Assess the morphology of the red blood cells.
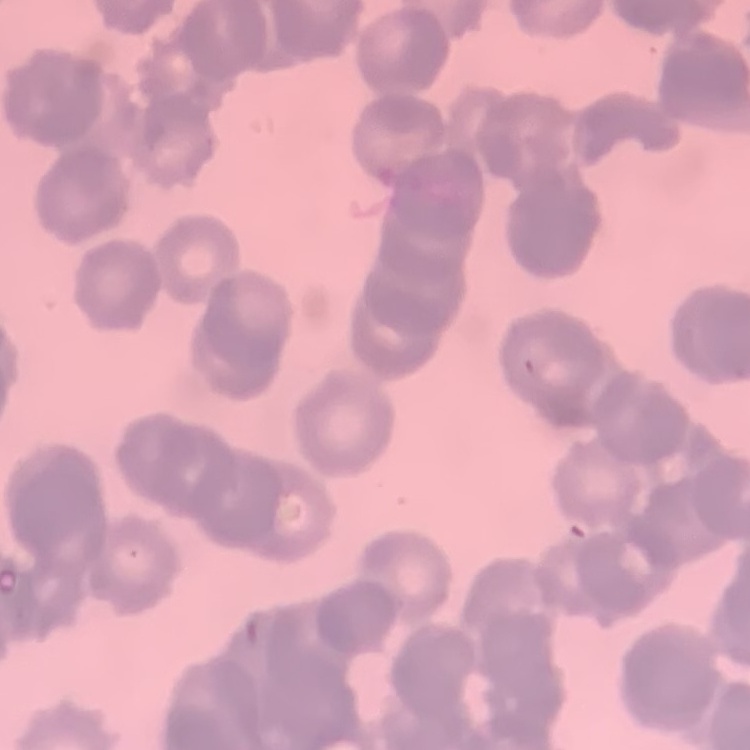

They show rouleaux formation.

Summary:
  - Image type: one tile cut from a larger photomicrograph
  - Preparation: thin peripheral smear
  - Stain: Field's or Giemsa